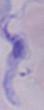
magnification = 1000x
identification = trypanosome
modality = micrograph